Classify this cell by malaria status.
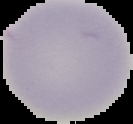
Uninfected.

Summary:
  - Image size: 133×124 pixels
  - Preparation: thin blood smear
  - Image type: segmented cell region with the area outside set to black